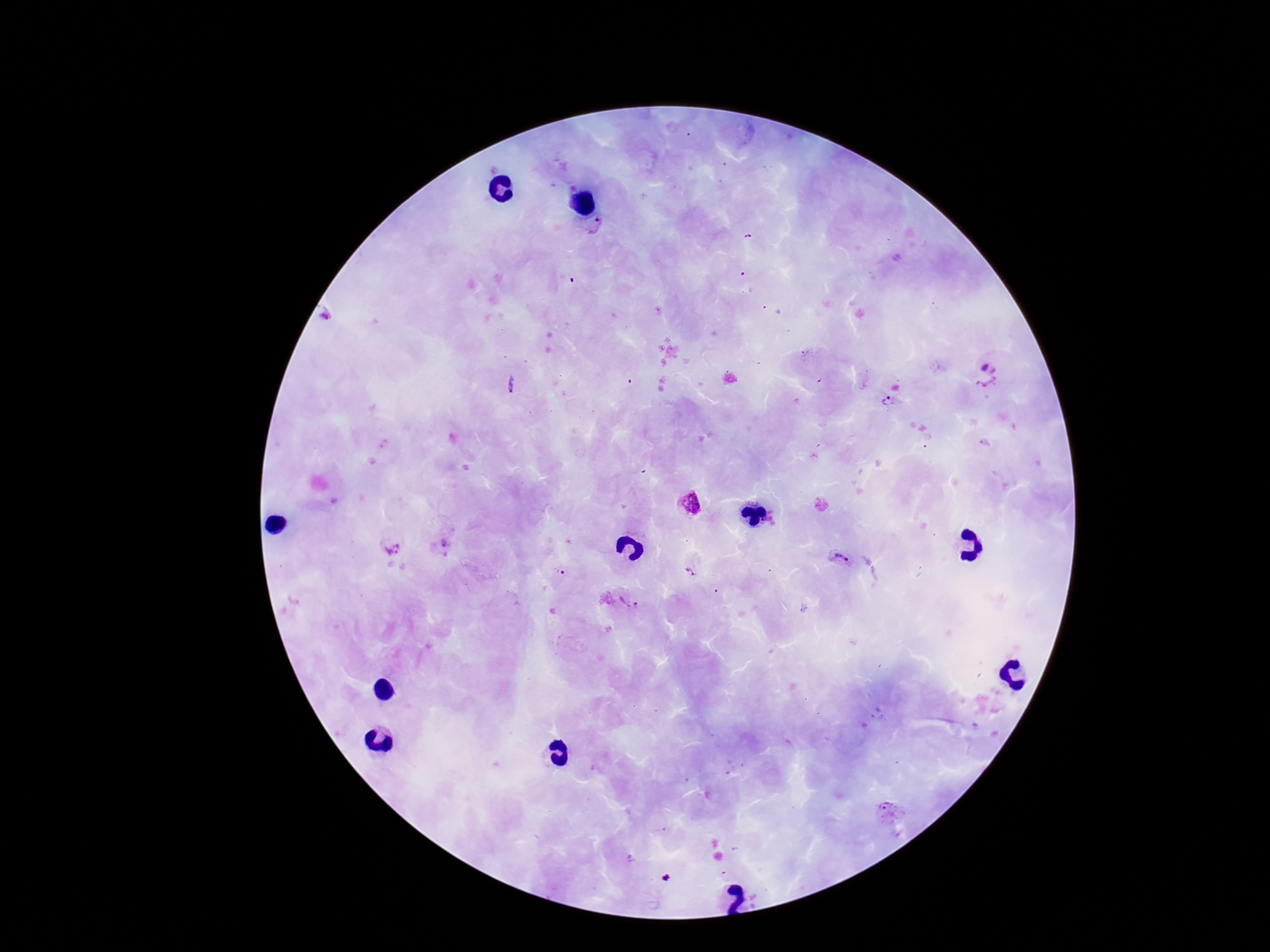

Approximate object centers, in pixels from the top-left corner. Plasmodium parasite locations: (x=600, y=227), (x=986, y=378), (x=888, y=404), (x=689, y=503), (x=445, y=544), (x=393, y=548), (x=842, y=559), (x=692, y=569), (x=558, y=574), (x=631, y=603), (x=887, y=811). Thick blood film. Image is 1270×952 pixels. 100x magnification. One field from this slide. Giemsa stain. Patient malaria status: positive. Smartphone photograph taken through the microscope eyepiece.